State which parasite is depicted.
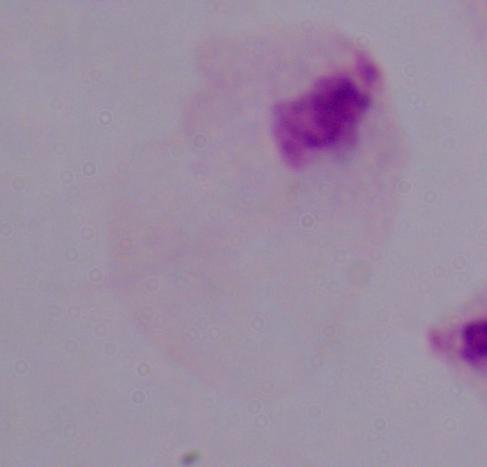
A trichomonad.

magnification: 1000x
modality: micrograph